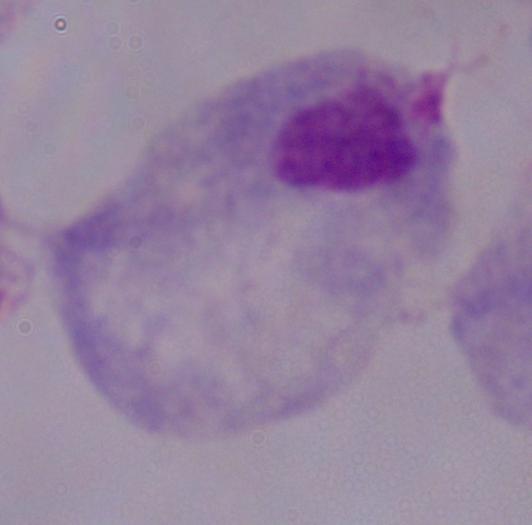

Summary:
  - Modality: photomicrograph
  - Identification: trichomonad
  - Magnification: 1000x